Evaluate for malaria.
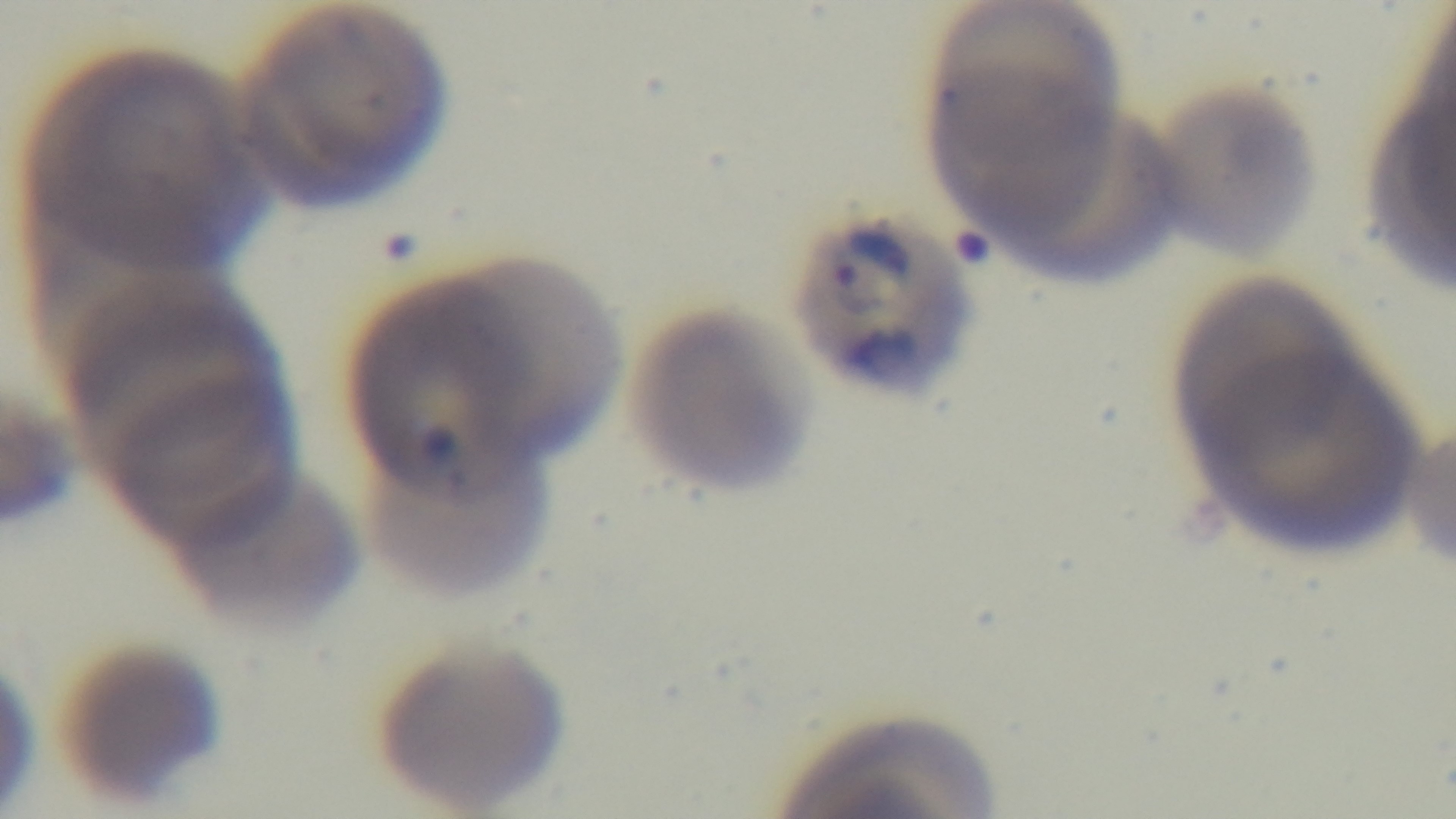
It is infected.

preparation = thin
modality = light microscopy
objective = 100x oil immersion
field of view = one from the slide
capture = mounted 4K digital camera
stain = Giemsa